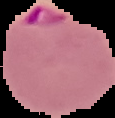
Summary:
  - Preparation: thin blood film
  - Image type: cell region segmented out of the field of view; surrounding area masked to black
  - Result: Plasmodium parasites identified
  - Image size: 115×118 pixels